Assess this cell for malaria.
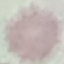
It is uninfected.

preparation = thin smear
capture = smartphone through the microscope eyepiece
stain = Giemsa
image type = automatically extracted cell patch, resized to 64 × 64 pixels